Report the malaria status of this cell.
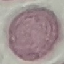

It is uninfected.

Summary:
  - Stain: Giemsa
  - Preparation: thin blood smear
  - Capture: smartphone through the microscope eyepiece
  - Image type: automatically extracted cell patch, resized to 64 × 64 pixels